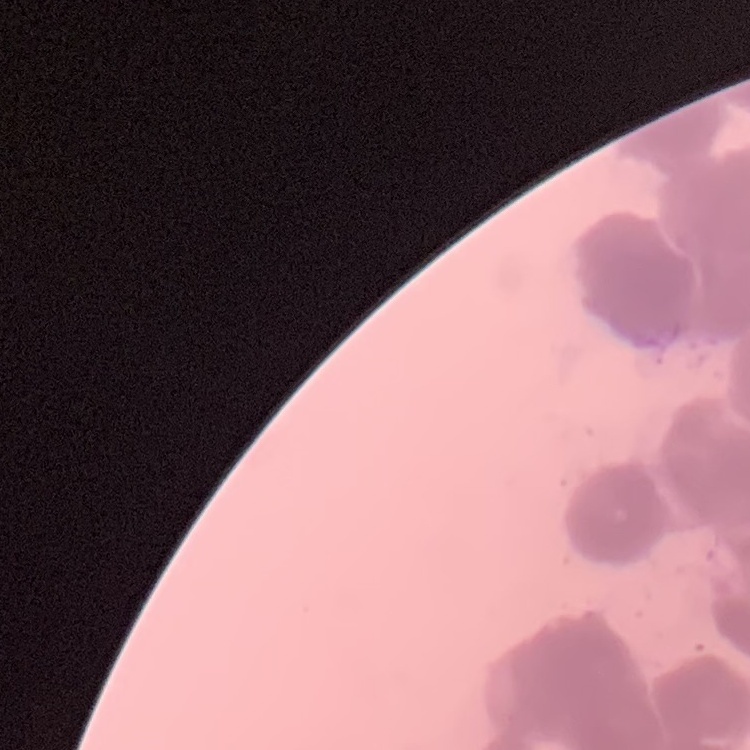
The erythrocytes show rouleaux formation. Square crop of a larger photomicrograph. Thin peripheral smear. Field's or Giemsa stain.